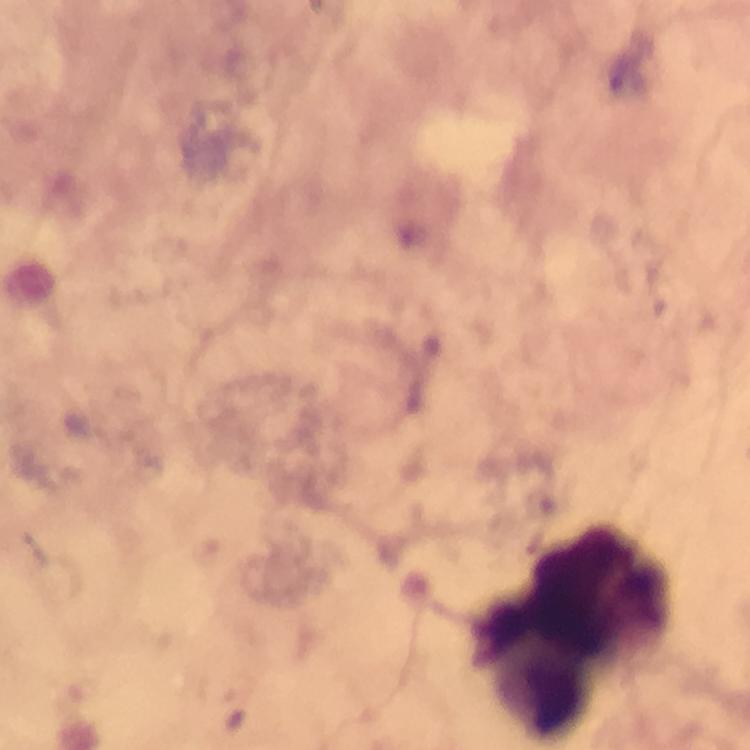

preparation = thick blood film
capture = smartphone mounted on the microscope
context = from a diagnostic examination for malaria
cropped from = a single field of view
malaria parasites = none seen
leukocyte locations = approximate centers as {x, y} in pixels: {578, 633}
magnification = 100x
stain = Giemsa
image size = 750×750 pixels
immersion oil = used